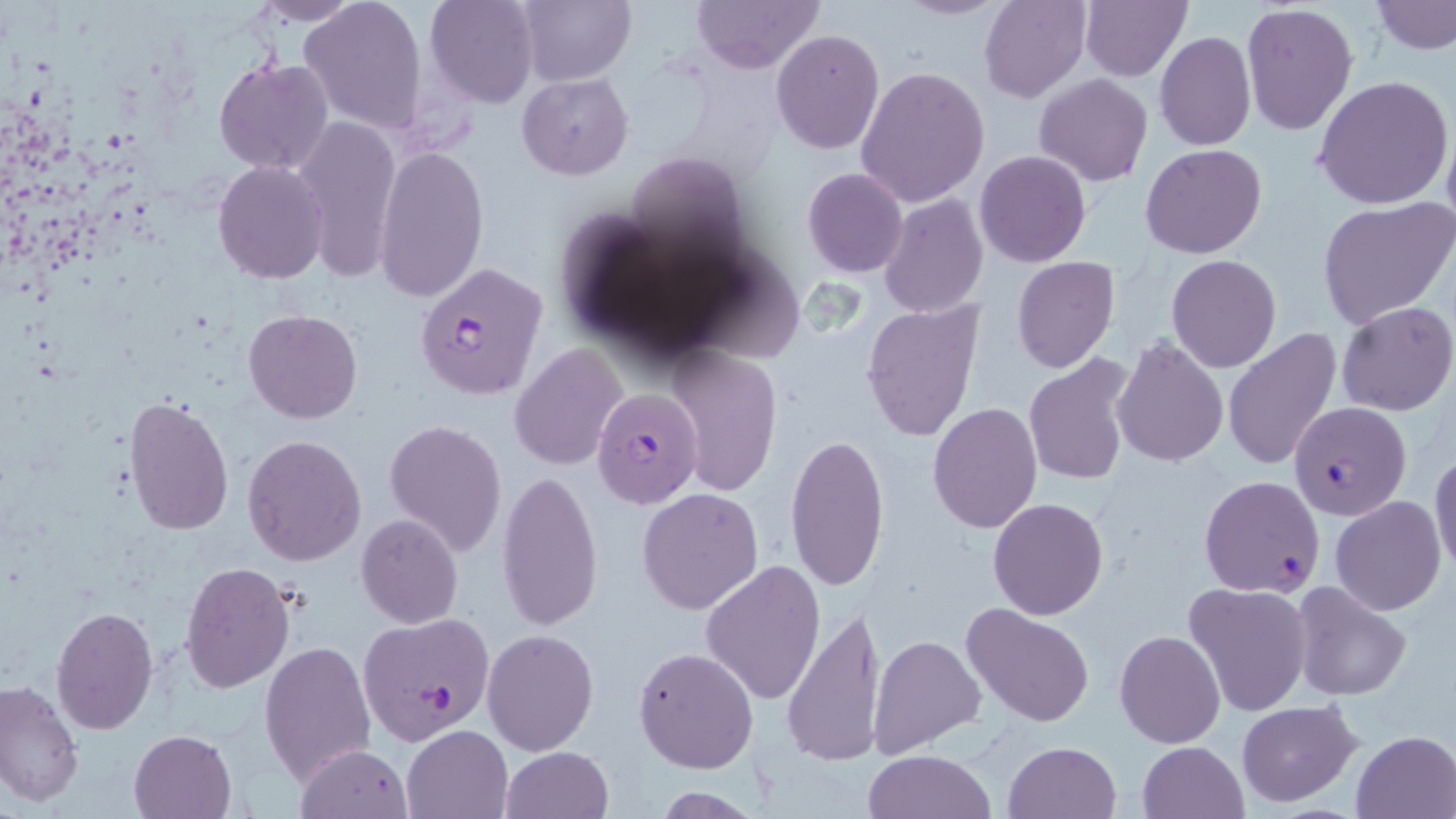

Summary:
  - Coordinate format: approximate bounding boxes as (x1, y1, x2, y2) in pixels
  - Uninfected red blood cell locations: (248, 0, 361, 24), (299, 0, 428, 132), (425, 0, 540, 108), (518, 0, 635, 86), (692, 0, 823, 73), (895, 0, 1010, 20), (980, 0, 1090, 102), (1080, 0, 1190, 80), (1372, 0, 1456, 55), (1240, 4, 1357, 135), (771, 30, 884, 153), (1155, 31, 1255, 150), (213, 59, 333, 175), (856, 65, 989, 208), (517, 72, 633, 179), (1034, 75, 1153, 186), (1313, 76, 1455, 211), (291, 113, 402, 281), (1441, 119, 1456, 239), (1142, 144, 1266, 259), (375, 145, 486, 303), (974, 151, 1091, 267), (213, 160, 329, 284), (802, 168, 909, 278), (878, 194, 989, 319), (1317, 197, 1456, 329), (1165, 255, 1282, 373), (1012, 257, 1118, 373), (860, 299, 986, 444), (1336, 302, 1456, 417), (244, 309, 362, 423), (1222, 326, 1344, 473), (1113, 337, 1229, 467), (510, 343, 629, 470), (665, 346, 784, 496), (1023, 356, 1138, 488), (124, 395, 235, 537), (928, 402, 1042, 534), (384, 418, 508, 556), (783, 431, 891, 594), (242, 434, 367, 566), (1429, 449, 1456, 578), (498, 468, 604, 633), (637, 486, 764, 614), (1331, 497, 1446, 615), (988, 498, 1109, 620), (356, 514, 463, 628), (699, 561, 826, 707), (179, 563, 295, 693), (1287, 581, 1413, 702), (1182, 582, 1312, 718), (960, 602, 1095, 729), (50, 604, 158, 734), (780, 604, 889, 768), (483, 628, 599, 756), (1114, 628, 1225, 748), (868, 633, 987, 759), (260, 640, 376, 785), (633, 646, 759, 773), (0, 681, 82, 809), (1235, 699, 1362, 804), (403, 726, 512, 818), (129, 729, 237, 818), (1351, 730, 1456, 817), (1002, 741, 1123, 819), (1138, 741, 1248, 818), (297, 744, 411, 817), (502, 746, 613, 819), (865, 749, 996, 819), (649, 788, 763, 817)
  - Plasmodium falciparum-infected red blood cell locations: (414, 263, 549, 398), (593, 386, 704, 508), (1289, 401, 1412, 521), (1198, 475, 1325, 598), (357, 613, 496, 745)
  - Slide-level diagnosis: Plasmodium falciparum
  - Modality: optical microscopy
  - Field of view: one of a larger specimen
  - Magnification: 1000x
  - Stain: May-Grünwald-Giemsa
  - Preparation: thin blood film
  - Image size: 1456×819 pixels